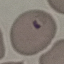
Summary:
  - Malaria status: parasitized
  - Stain: Giemsa
  - Capture: smartphone through the microscope eyepiece
  - Preparation: thin blood smear
  - Image type: cell patch, automatically extracted from a larger field of view and resized to 64 × 64 pixels